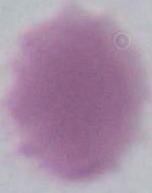
identification: red blood cell
modality: micrograph
magnification: 1000x